Locate every blood parasite and identify its species.
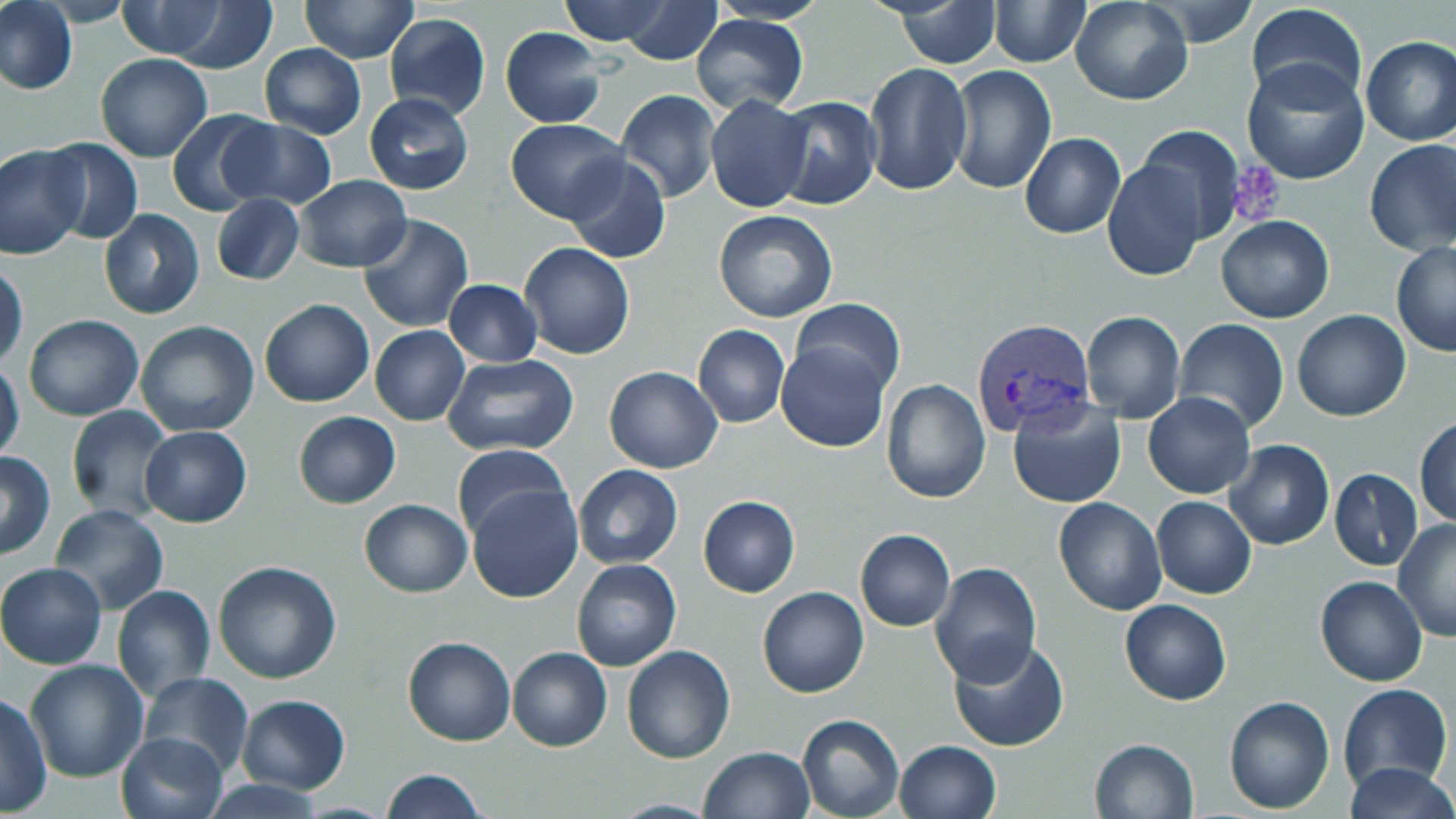
Approximate bounding boxes as named x1/y1/x2/y2 corners in pixels.
Plasmodium vivax-infected red blood cells: (x1=971, y1=318, x2=1095, y2=437).
No Plasmodium falciparum, Plasmodium ovale, Plasmodium malariae, Babesia divergens, or Trypanosoma brucei observed.

Summary:
  - Platelet locations: (x1=1231, y1=163, x2=1285, y2=226)
  - Uninfected red blood cell locations: (x1=0, y1=0, x2=78, y2=97), (x1=300, y1=0, x2=417, y2=64), (x1=559, y1=0, x2=673, y2=46), (x1=617, y1=0, x2=722, y2=65), (x1=990, y1=0, x2=1089, y2=67), (x1=1070, y1=0, x2=1194, y2=105), (x1=891, y1=1, x2=1003, y2=67), (x1=1145, y1=1, x2=1258, y2=47), (x1=144, y1=2, x2=280, y2=71), (x1=1245, y1=2, x2=1369, y2=108), (x1=111, y1=3, x2=227, y2=60), (x1=385, y1=12, x2=490, y2=121), (x1=692, y1=14, x2=808, y2=114), (x1=499, y1=27, x2=606, y2=128), (x1=1360, y1=35, x2=1456, y2=146), (x1=260, y1=43, x2=366, y2=138), (x1=96, y1=52, x2=213, y2=162), (x1=1240, y1=58, x2=1370, y2=185), (x1=863, y1=63, x2=971, y2=195), (x1=948, y1=65, x2=1057, y2=194), (x1=615, y1=90, x2=722, y2=203), (x1=364, y1=91, x2=474, y2=194), (x1=705, y1=94, x2=811, y2=213), (x1=770, y1=96, x2=883, y2=209), (x1=167, y1=108, x2=275, y2=217), (x1=218, y1=119, x2=339, y2=209), (x1=505, y1=119, x2=628, y2=222), (x1=1135, y1=125, x2=1246, y2=244), (x1=1019, y1=133, x2=1126, y2=239), (x1=37, y1=139, x2=143, y2=243), (x1=1364, y1=139, x2=1456, y2=256), (x1=0, y1=144, x2=87, y2=259), (x1=563, y1=155, x2=671, y2=264), (x1=1102, y1=159, x2=1207, y2=282), (x1=294, y1=176, x2=411, y2=271), (x1=211, y1=194, x2=304, y2=286), (x1=98, y1=209, x2=205, y2=320), (x1=714, y1=211, x2=838, y2=323), (x1=356, y1=214, x2=473, y2=332), (x1=1215, y1=215, x2=1336, y2=323), (x1=1391, y1=241, x2=1456, y2=357), (x1=518, y1=242, x2=636, y2=360), (x1=1, y1=261, x2=27, y2=366), (x1=443, y1=279, x2=542, y2=368), (x1=789, y1=297, x2=905, y2=397), (x1=259, y1=299, x2=374, y2=407), (x1=1080, y1=311, x2=1186, y2=424), (x1=1292, y1=311, x2=1411, y2=422), (x1=23, y1=314, x2=144, y2=421), (x1=1174, y1=319, x2=1290, y2=434), (x1=134, y1=320, x2=260, y2=438), (x1=693, y1=324, x2=790, y2=429), (x1=369, y1=325, x2=470, y2=425), (x1=776, y1=340, x2=890, y2=452), (x1=442, y1=353, x2=579, y2=456), (x1=0, y1=359, x2=24, y2=465), (x1=603, y1=365, x2=722, y2=474), (x1=882, y1=378, x2=991, y2=503), (x1=1143, y1=392, x2=1256, y2=498), (x1=1007, y1=395, x2=1126, y2=509), (x1=65, y1=405, x2=174, y2=522), (x1=293, y1=411, x2=401, y2=509), (x1=1414, y1=416, x2=1456, y2=526), (x1=139, y1=425, x2=252, y2=528), (x1=1225, y1=440, x2=1334, y2=550), (x1=452, y1=444, x2=574, y2=544), (x1=1, y1=451, x2=54, y2=560), (x1=572, y1=464, x2=683, y2=568), (x1=1330, y1=470, x2=1422, y2=569), (x1=466, y1=484, x2=582, y2=603), (x1=698, y1=496, x2=800, y2=597), (x1=1053, y1=496, x2=1166, y2=615), (x1=1151, y1=496, x2=1257, y2=599), (x1=358, y1=498, x2=472, y2=597), (x1=48, y1=504, x2=170, y2=614), (x1=1392, y1=519, x2=1456, y2=643), (x1=855, y1=529, x2=955, y2=631), (x1=213, y1=560, x2=343, y2=685), (x1=572, y1=560, x2=681, y2=670), (x1=1, y1=562, x2=107, y2=669), (x1=930, y1=562, x2=1041, y2=685), (x1=1315, y1=576, x2=1427, y2=686), (x1=111, y1=584, x2=216, y2=700), (x1=757, y1=586, x2=869, y2=698), (x1=1120, y1=599, x2=1231, y2=705), (x1=402, y1=636, x2=516, y2=747), (x1=948, y1=637, x2=1069, y2=753), (x1=621, y1=645, x2=736, y2=766), (x1=507, y1=648, x2=612, y2=751), (x1=24, y1=659, x2=149, y2=783), (x1=136, y1=671, x2=252, y2=776), (x1=1339, y1=683, x2=1452, y2=794), (x1=0, y1=692, x2=51, y2=815), (x1=236, y1=695, x2=351, y2=794), (x1=1223, y1=695, x2=1336, y2=814), (x1=797, y1=714, x2=904, y2=819), (x1=116, y1=732, x2=227, y2=819), (x1=1089, y1=737, x2=1198, y2=819), (x1=893, y1=739, x2=1001, y2=819), (x1=701, y1=744, x2=814, y2=819), (x1=1341, y1=762, x2=1456, y2=819), (x1=381, y1=769, x2=488, y2=818), (x1=200, y1=779, x2=330, y2=817)
  - Slide-level diagnosis: Plasmodium vivax
  - Modality: optical microscopy
  - Preparation: thin blood film
  - Image size: 1456×819 pixels
  - Magnification: 1000x
  - Field of view: one of a larger specimen
  - Stain: May-Grünwald-Giemsa